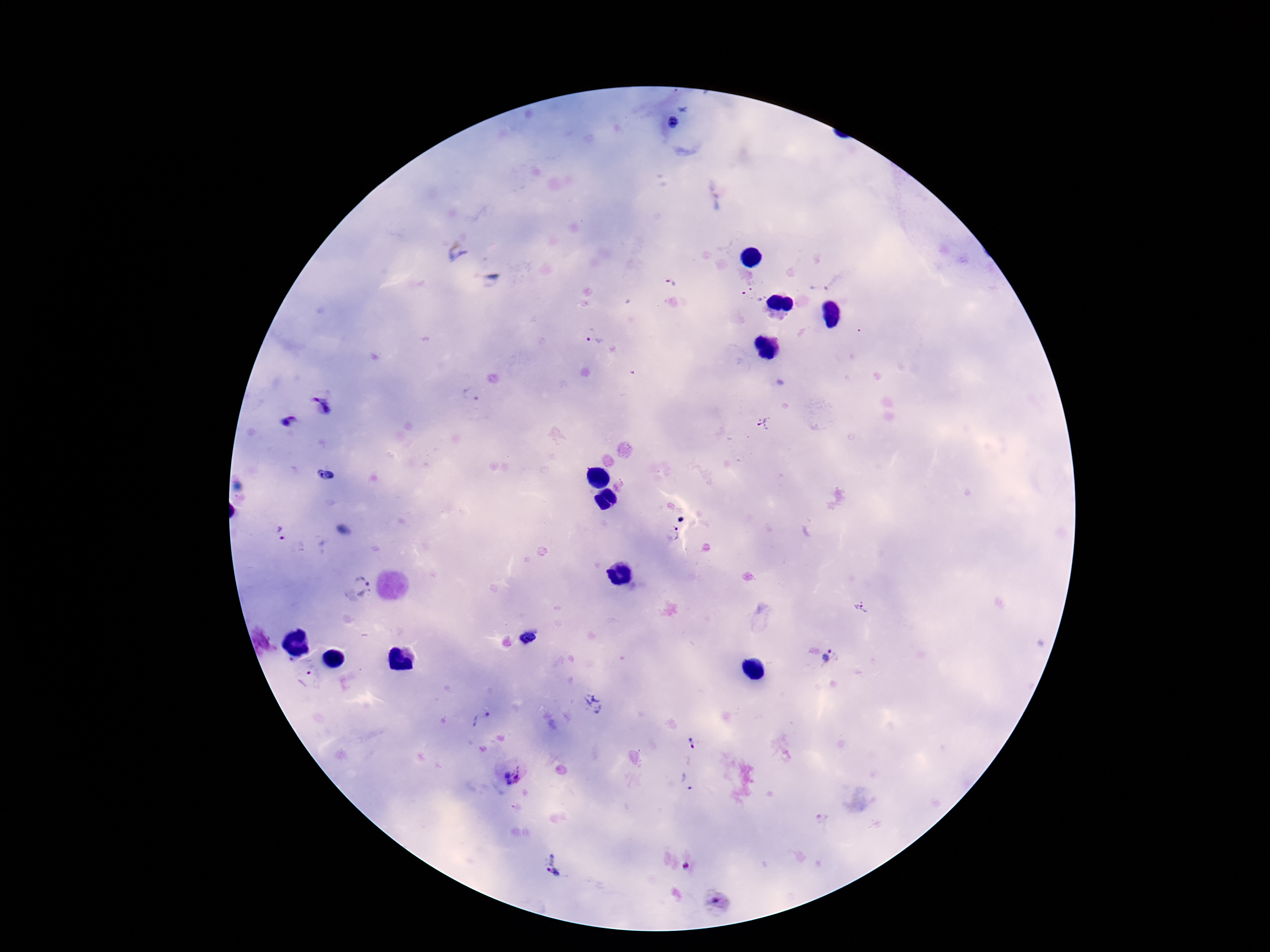
Approximate object centers, in pixels from the top-left corner.
Summary:
  - Plasmodium parasite locations: (x=672, y=123), (x=456, y=251), (x=670, y=283), (x=819, y=287), (x=753, y=296), (x=593, y=337), (x=470, y=395), (x=323, y=406), (x=291, y=422), (x=762, y=425), (x=326, y=475), (x=679, y=518), (x=280, y=534), (x=673, y=535), (x=363, y=585), (x=862, y=608), (x=529, y=639), (x=830, y=657), (x=307, y=677), (x=594, y=704), (x=483, y=722), (x=691, y=742), (x=514, y=774), (x=685, y=783), (x=553, y=865), (x=685, y=866), (x=718, y=903)
  - Field of view: one from this slide
  - Magnification: 100x
  - Preparation: thick blood smear
  - Image size: 1270×952 pixels
  - Stain: Giemsa
  - Patient malaria status: positive
  - Capture: smartphone camera through the microscope eyepiece